Give the preparation type.
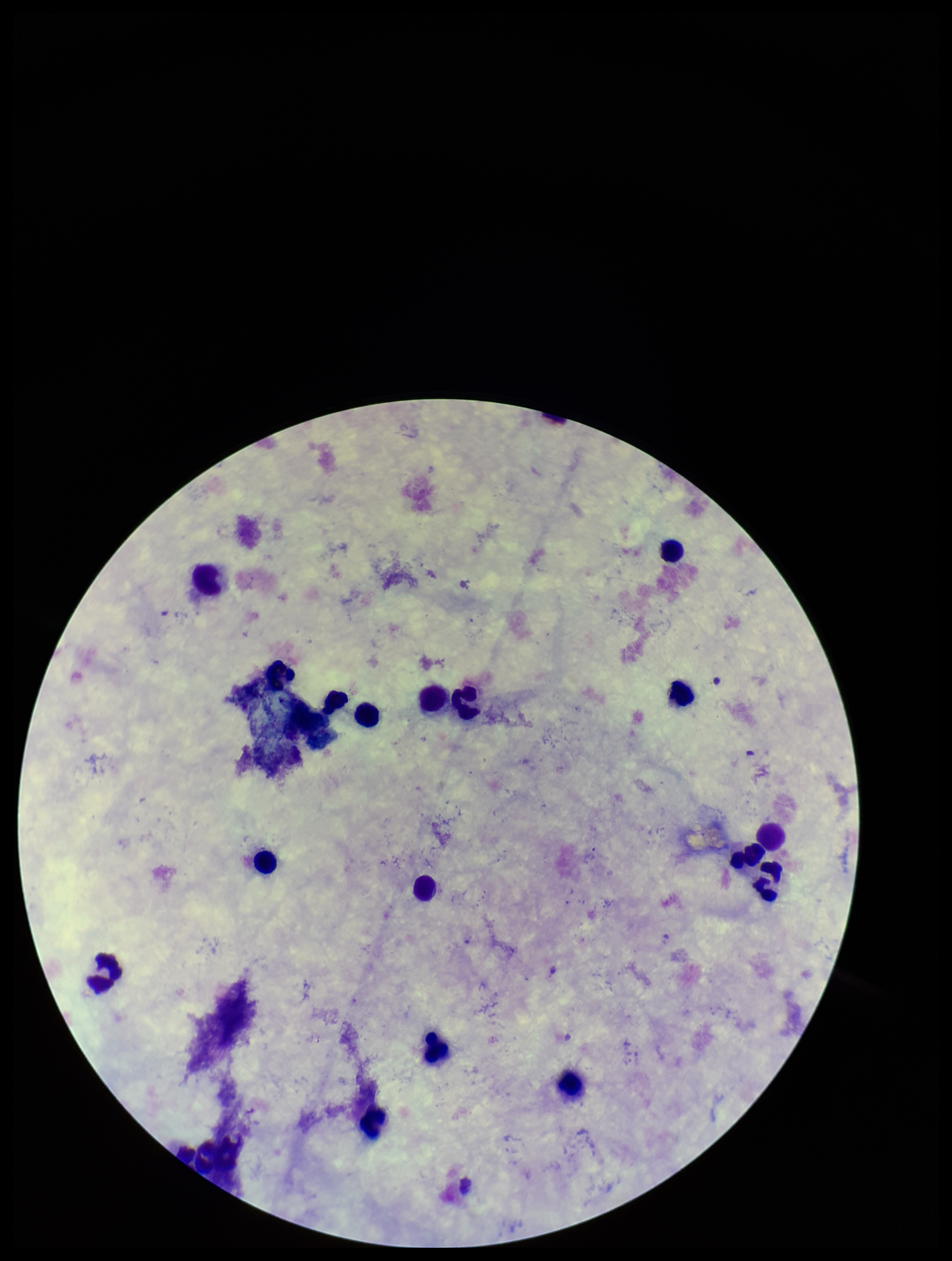

A thick smear.

{
  "plasmodium_parasites": "none detected",
  "leukocyte_count": 17,
  "field_of_view": "one from this slide",
  "stain": "Giemsa",
  "capture": "smartphone photograph through the microscope eyepiece",
  "parasite_count": 0,
  "patient_malaria_status": "negative",
  "image_size": "952×1261 pixels"
}